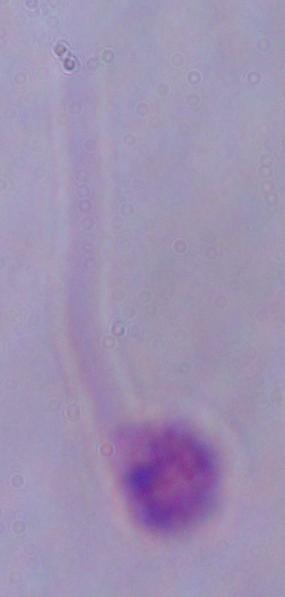
magnification = 1000x
modality = photomicrograph
identification = Leishmania